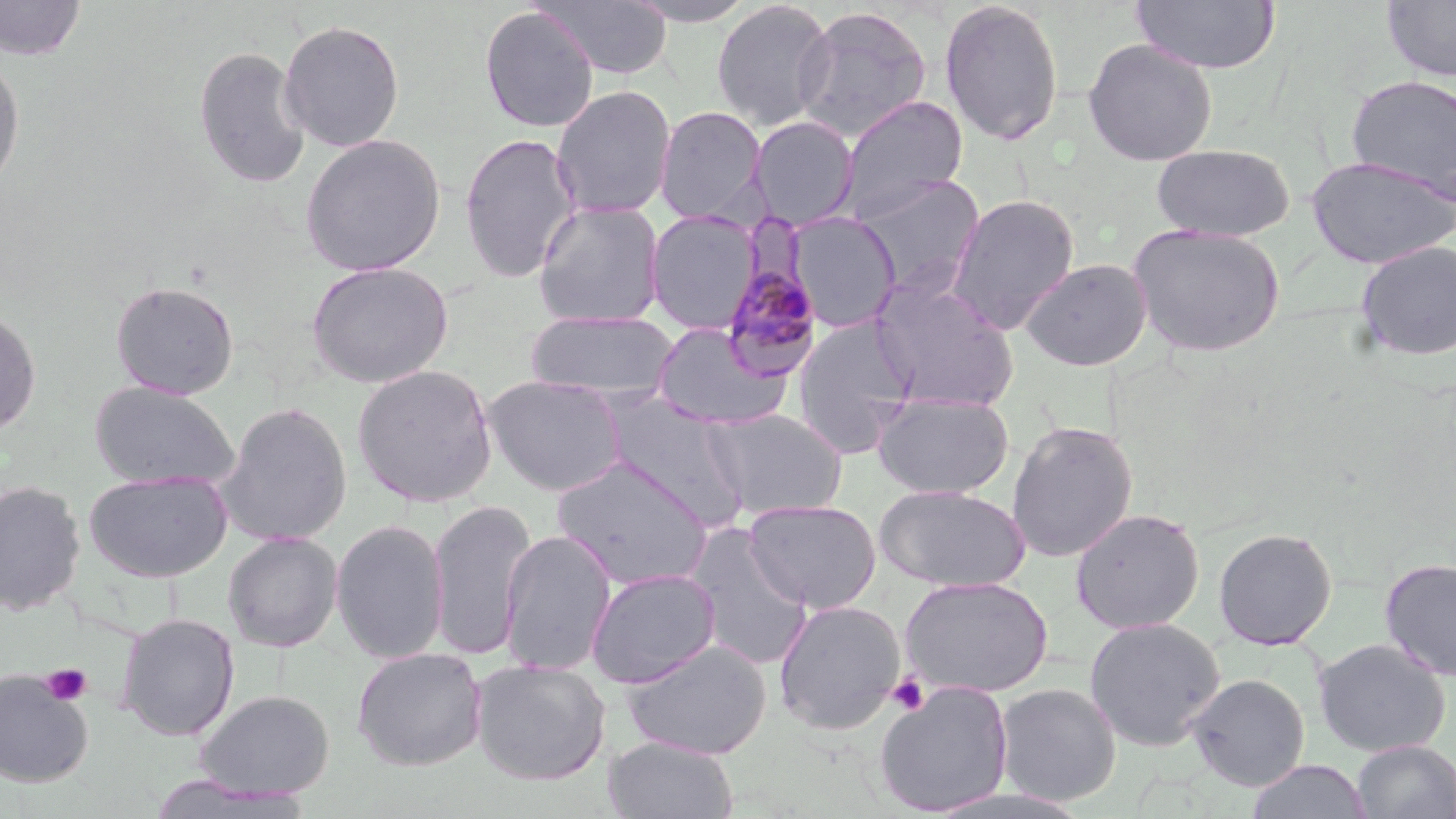

{
  "slide_level_diagnosis": "Plasmodium malariae",
  "stain": "May-Grünwald-Giemsa",
  "field_of_view": "single",
  "magnification": "1000x",
  "preparation": "thin blood film",
  "modality": "optical microscopy",
  "plasmodium_malariae_infected_red_blood_cell_locations": "approximate bounding boxes as (x1,y1)-(x2,y2) corner pairs in pixels: (721,257)-(824,381)",
  "uninfected_red_blood_cell_locations": "approximate bounding boxes as (x1,y1)-(x2,y2) corner pairs in pixels: (1,0)-(88,61), (535,0)-(674,80), (622,0)-(761,26), (711,0)-(836,132), (938,0)-(1065,147), (1130,0)-(1281,75), (1381,0)-(1456,83), (478,6)-(599,133), (792,6)-(933,144), (278,19)-(405,153), (1082,38)-(1218,166), (193,45)-(311,191), (0,53)-(25,195), (1345,74)-(1456,203), (551,85)-(677,219), (838,96)-(968,220), (655,106)-(767,223), (749,116)-(859,230), (459,131)-(582,283), (299,134)-(446,277), (1151,143)-(1296,241), (1305,155)-(1455,269), (853,174)-(985,296), (946,193)-(1080,335), (533,201)-(665,327), (646,210)-(760,334), (787,211)-(902,333), (1128,223)-(1285,358), (1354,240)-(1456,361), (1020,258)-(1152,371), (306,260)-(454,389), (868,274)-(1020,411), (109,280)-(240,400), (0,306)-(41,438), (527,309)-(681,403), (792,316)-(918,457), (652,322)-(792,430), (352,363)-(498,507), (483,374)-(628,496), (89,380)-(239,490), (872,393)-(1014,498), (602,394)-(747,527), (216,401)-(352,546), (704,408)-(848,520), (1006,420)-(1138,562), (552,456)-(715,590), (83,470)-(233,582), (0,480)-(86,617), (874,484)-(1031,593), (428,498)-(536,661), (744,499)-(882,614), (1070,507)-(1205,634), (331,518)-(450,665), (683,523)-(814,671), (1213,527)-(1338,650), (499,528)-(617,676), (222,531)-(343,652), (1380,557)-(1456,680), (585,567)-(721,687), (900,575)-(1053,698), (773,599)-(906,735), (116,612)-(240,741), (1084,617)-(1226,751), (621,638)-(772,759), (1313,638)-(1450,757), (351,646)-(487,771), (470,659)-(611,786), (0,668)-(94,787), (1186,672)-(1310,791), (873,680)-(1014,817), (993,683)-(1122,806), (194,689)-(335,798), (603,736)-(739,819), (1351,740)-(1456,819), (1246,759)-(1370,818)",
  "image_size": "1456×819 pixels",
  "platelet_locations": "approximate bounding boxes as (x1,y1)-(x2,y2) corner pairs in pixels: (40,663)-(93,707), (886,674)-(929,715)"
}